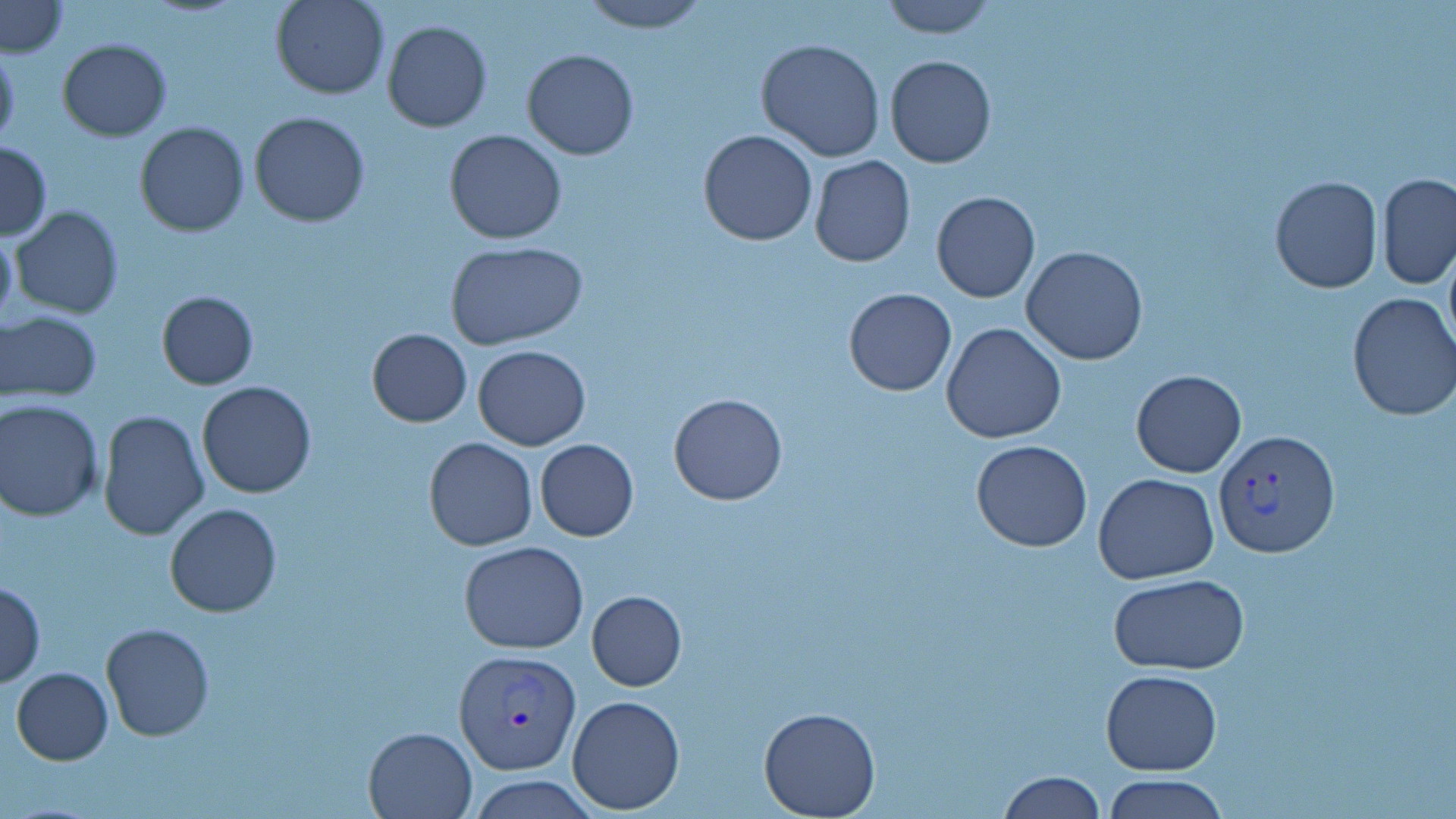
slide-level diagnosis = Plasmodium vivax
field of view = one of a larger specimen
preparation = thin blood smear
magnification = 1000x
modality = light microscopy
uninfected red blood cell locations = approximate bounding boxes as (x1, y1, x2, y2) in pixels: (271, 0, 390, 99), (578, 0, 711, 33), (875, 0, 999, 38), (2, 1, 69, 56), (382, 21, 492, 133), (57, 37, 173, 141), (756, 37, 886, 162), (0, 44, 21, 153), (522, 49, 638, 160), (885, 55, 995, 168), (248, 110, 372, 227), (135, 121, 250, 236), (443, 129, 567, 245), (699, 129, 817, 246), (1, 140, 52, 240), (809, 155, 916, 269), (1377, 172, 1456, 290), (1269, 175, 1382, 293), (931, 191, 1040, 303), (11, 206, 123, 318), (0, 225, 17, 331), (445, 241, 588, 350), (1443, 241, 1456, 361), (1022, 246, 1149, 366), (844, 288, 957, 396), (156, 290, 259, 388), (1346, 292, 1456, 422), (1, 308, 103, 404), (941, 321, 1068, 444), (366, 327, 472, 427), (366, 337, 589, 439), (472, 345, 592, 450), (1130, 370, 1247, 477), (196, 381, 318, 500), (668, 392, 789, 506), (0, 398, 104, 521), (97, 410, 209, 540), (423, 436, 539, 551), (534, 438, 639, 541), (971, 440, 1093, 551), (1093, 473, 1220, 584), (165, 502, 282, 617), (459, 540, 589, 653), (1110, 574, 1248, 674), (0, 581, 45, 687), (586, 591, 687, 691), (100, 623, 214, 742), (10, 667, 113, 765), (1100, 670, 1223, 774), (566, 694, 685, 813), (758, 707, 882, 819), (363, 726, 476, 818), (997, 772, 1107, 818), (1103, 774, 1229, 819), (469, 775, 598, 818)
stain = May-Grünwald-Giemsa
image size = 1456×819 pixels
Plasmodium vivax-infected red blood cell locations = approximate bounding boxes as (x1, y1, x2, y2) in pixels: (1213, 427, 1342, 560), (454, 649, 580, 776)